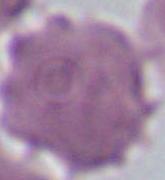

magnification = 1000x
modality = micrograph
identification = erythrocyte